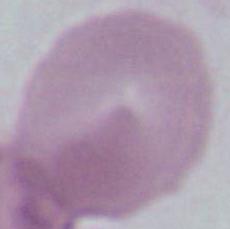

magnification: 400x or 1000x
identification: Plasmodium
modality: micrograph